Assess this cell for malaria.
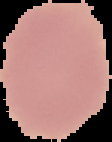
It is uninfected.

Summary:
  - Image size: 112×142 pixels
  - Preparation: thin blood smear
  - Image type: segmented cell region on a black background